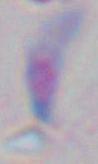

1000x magnification. Toxoplasma gondii is shown. Photomicrograph.